Name the blood parasite species.
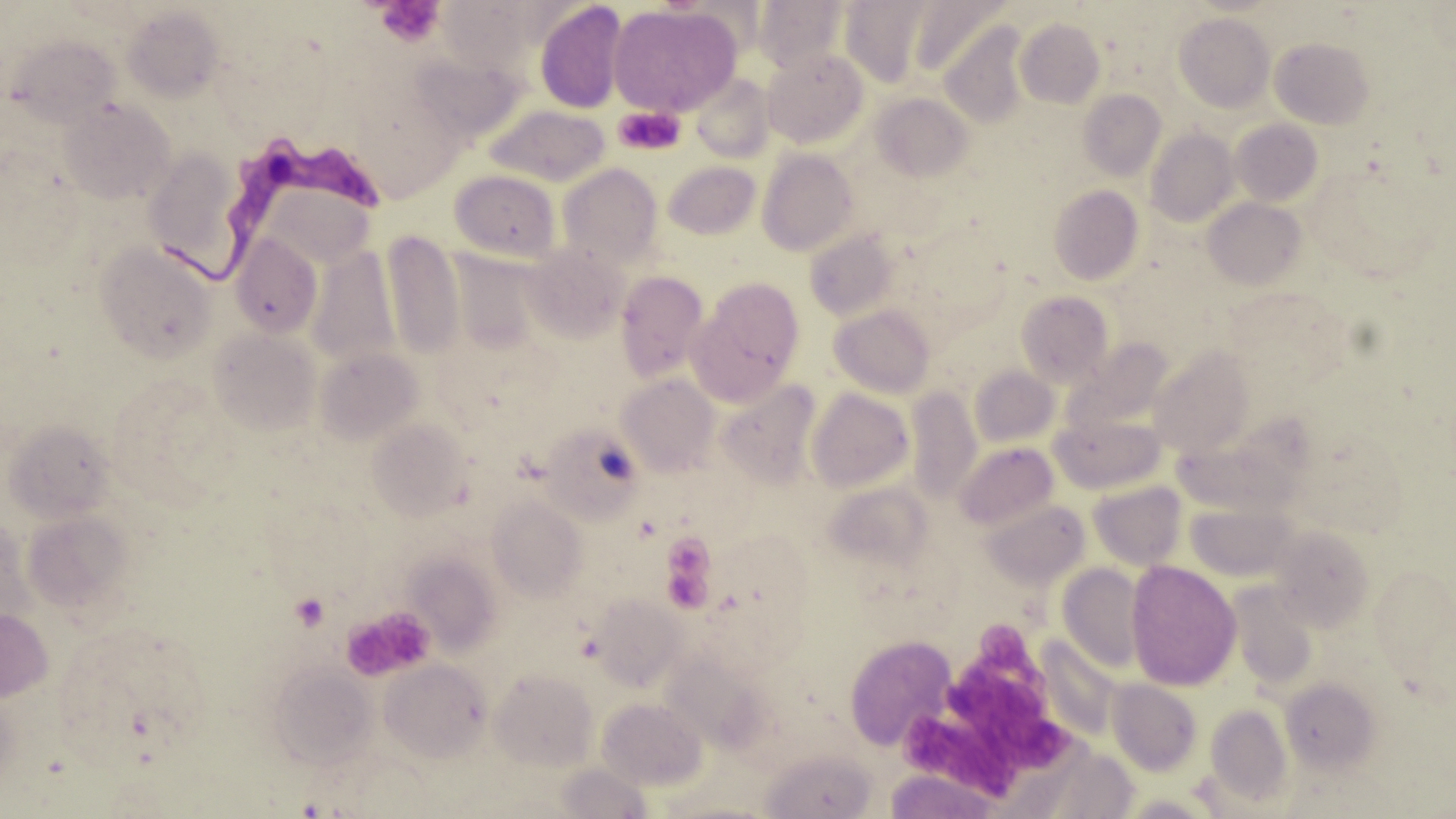
Trypanosoma brucei.

{
  "field_of_view": "one of a larger specimen",
  "trypanosoma_brucei_locations": "approximate bounding boxes as [x1, y1, x2, y2] in pixels: [161, 137, 383, 290]",
  "modality": "optical microscopy",
  "preparation": "thin blood smear",
  "stain": "May-Grünwald-Giemsa",
  "platelet_locations": "approximate bounding boxes as [x1, y1, x2, y2] in pixels: [376, 0, 443, 48], [613, 106, 686, 155], [664, 535, 713, 576], [669, 576, 711, 613], [291, 593, 330, 631], [343, 607, 434, 681], [971, 623, 1032, 682], [948, 664, 1042, 733], [989, 714, 1073, 773], [904, 720, 1015, 798]",
  "image_size": "1456×819 pixels",
  "uninfected_red_blood_cell_locations": "approximate bounding boxes as [x1, y1, x2, y2] in pixels: [754, 0, 847, 72], [534, 1, 628, 114], [840, 1, 930, 86], [906, 1, 1007, 78], [437, 2, 529, 73], [609, 4, 741, 116], [122, 5, 225, 103], [1174, 13, 1275, 112], [1015, 17, 1105, 107], [939, 22, 1030, 129], [6, 33, 121, 126], [1269, 36, 1374, 129], [762, 48, 868, 148], [691, 73, 776, 162], [1079, 89, 1166, 181], [871, 92, 973, 182], [59, 98, 176, 204], [483, 104, 610, 187], [1230, 119, 1323, 206], [1145, 128, 1238, 226], [144, 149, 252, 281], [757, 149, 860, 256], [663, 161, 761, 240], [557, 162, 664, 266], [450, 169, 561, 261], [269, 184, 374, 270], [1047, 185, 1143, 285], [1203, 197, 1307, 289], [381, 229, 465, 361], [803, 229, 902, 321], [231, 234, 323, 339], [95, 242, 219, 363], [523, 243, 628, 343], [306, 244, 401, 369], [615, 271, 710, 382], [690, 278, 804, 400], [1015, 290, 1114, 386], [829, 304, 936, 398], [209, 327, 322, 436], [1062, 339, 1173, 434], [1148, 344, 1255, 457], [314, 346, 423, 445], [969, 365, 1059, 449], [616, 374, 721, 476], [714, 380, 823, 487], [905, 387, 981, 503], [806, 388, 913, 492], [1051, 415, 1164, 493], [366, 418, 472, 520], [3, 420, 115, 523], [539, 423, 644, 523], [955, 442, 1058, 531], [1172, 442, 1290, 517], [1088, 481, 1186, 570], [820, 482, 934, 569], [487, 492, 588, 601], [982, 499, 1091, 589], [1187, 504, 1292, 581], [22, 510, 132, 615], [0, 518, 35, 625], [1270, 526, 1376, 634], [406, 553, 502, 654], [1126, 560, 1241, 690], [1058, 564, 1147, 672], [1227, 583, 1319, 691], [589, 593, 687, 689], [0, 607, 53, 702], [843, 634, 958, 750], [379, 658, 493, 762], [268, 663, 378, 770], [490, 668, 597, 770], [1280, 676, 1382, 773], [1107, 678, 1202, 775], [597, 697, 707, 790], [1205, 703, 1294, 807], [759, 747, 877, 819], [557, 762, 654, 818], [883, 769, 1007, 818]",
  "magnification": "1000x"
}